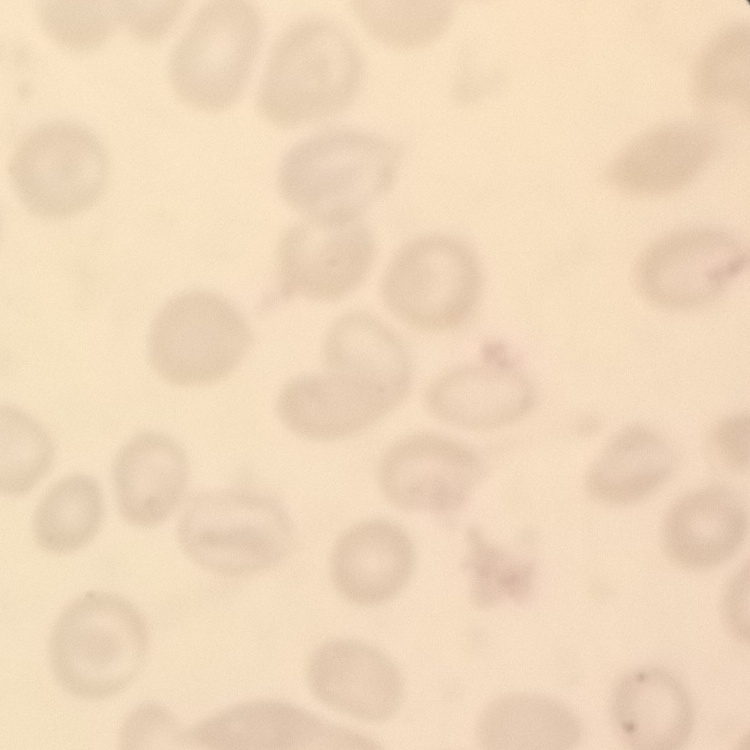 The erythrocytes show no rouleaux formation. Stained with either Field's or Giemsa. Thin blood smear. Square crop of a larger photomicrograph.